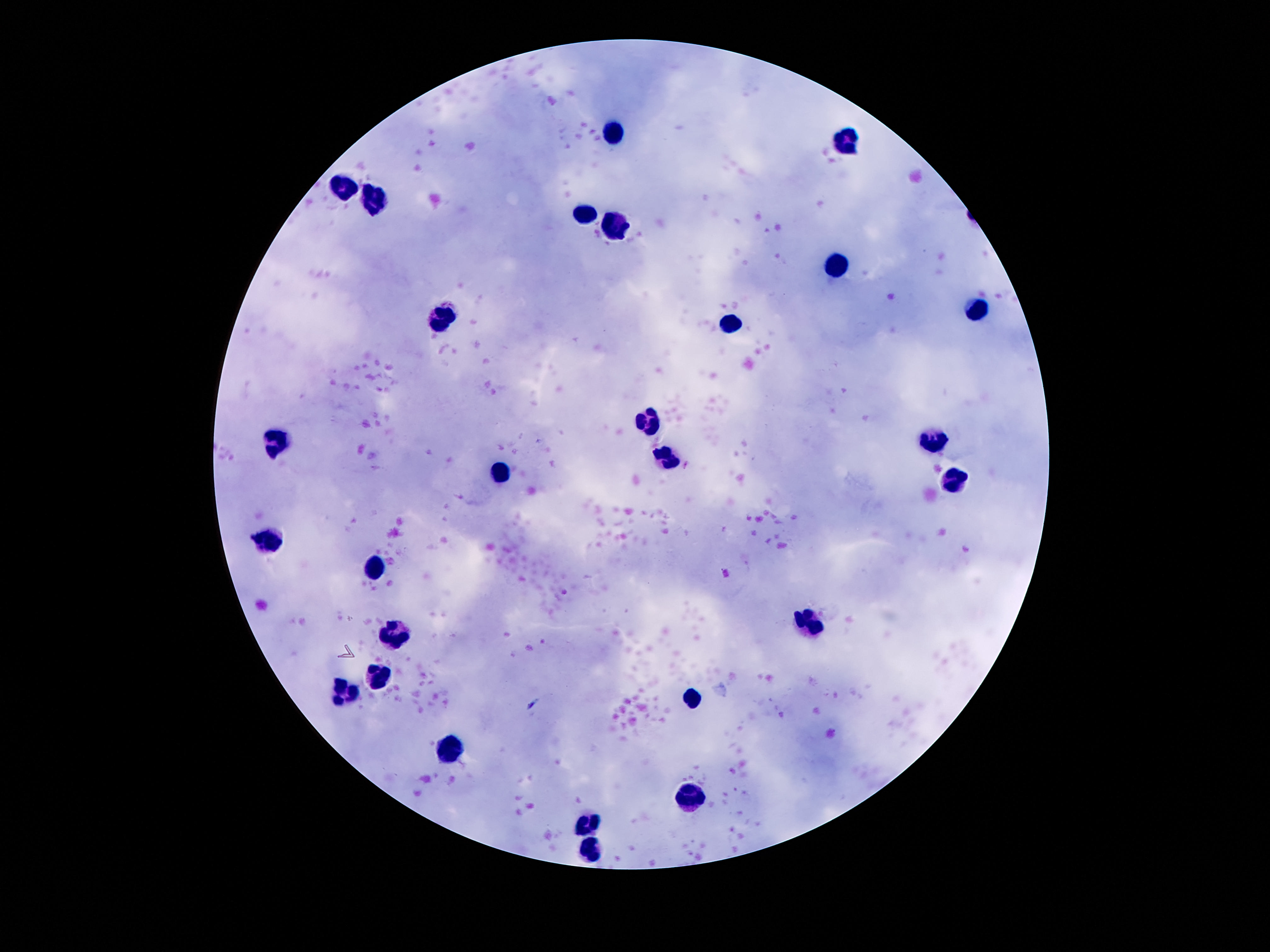

image size = 1270×952 pixels
preparation = thick blood film
capture = smartphone camera through the microscope eyepiece
stain = Giemsa
patient malaria status = negative
field of view = one from this slide
leukocyte locations = approximate centers as (x, y) in pixels: (614, 131), (844, 141), (342, 185), (379, 205), (583, 213), (616, 226), (835, 266), (975, 312), (441, 320), (732, 324), (650, 422), (278, 441), (936, 442), (667, 454), (500, 477), (954, 478), (271, 544), (373, 568), (812, 621), (396, 630), (379, 677), (345, 692), (689, 696), (452, 751), (687, 794), (592, 824), (590, 849)
magnification = 100x